State the preparation type.
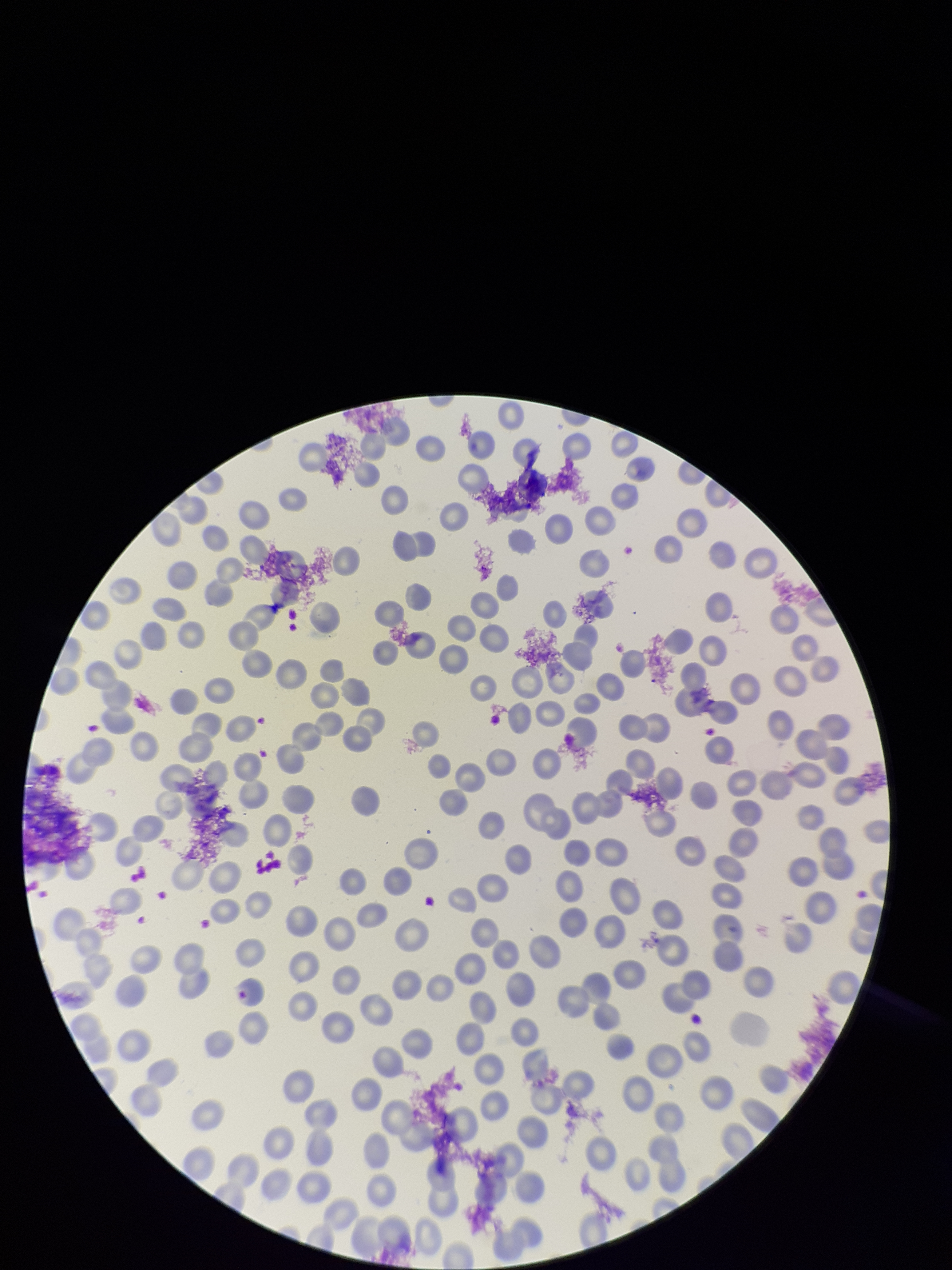
It is a thin blood smear.

Summary:
  - Red blood cell count: 241
  - Stain: Giemsa
  - Capture: smartphone photograph through the microscope eyepiece
  - Image size: 952×1270 pixels
  - Patient malaria status: negative
  - Parasitized red blood cells: none detected
  - Parasitized red blood cell count: 0
  - Field of view: single